Classify this cell by malaria status.
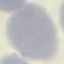
Uninfected.

Summary:
  - Preparation: thin blood film
  - Capture: smartphone camera at the microscope eyepiece
  - Image type: automatically extracted cell patch, resized to 64 × 64 pixels
  - Stain: Giemsa